Report the malaria status of this cell.
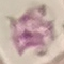

Uninfected.

Summary:
  - Image type: automatically extracted cell patch, resized to 64 × 64 pixels
  - Stain: Giemsa
  - Preparation: thin blood film
  - Capture: smartphone through the microscope eyepiece